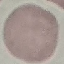

Summary:
  - Result: no malaria parasites seen
  - Preparation: thin blood smear
  - Image type: cell patch, automatically extracted from a larger field of view and resized to 64 × 64 pixels
  - Capture: smartphone through the microscope eyepiece
  - Stain: Giemsa